Give the extent of all uninfected red blood cells.
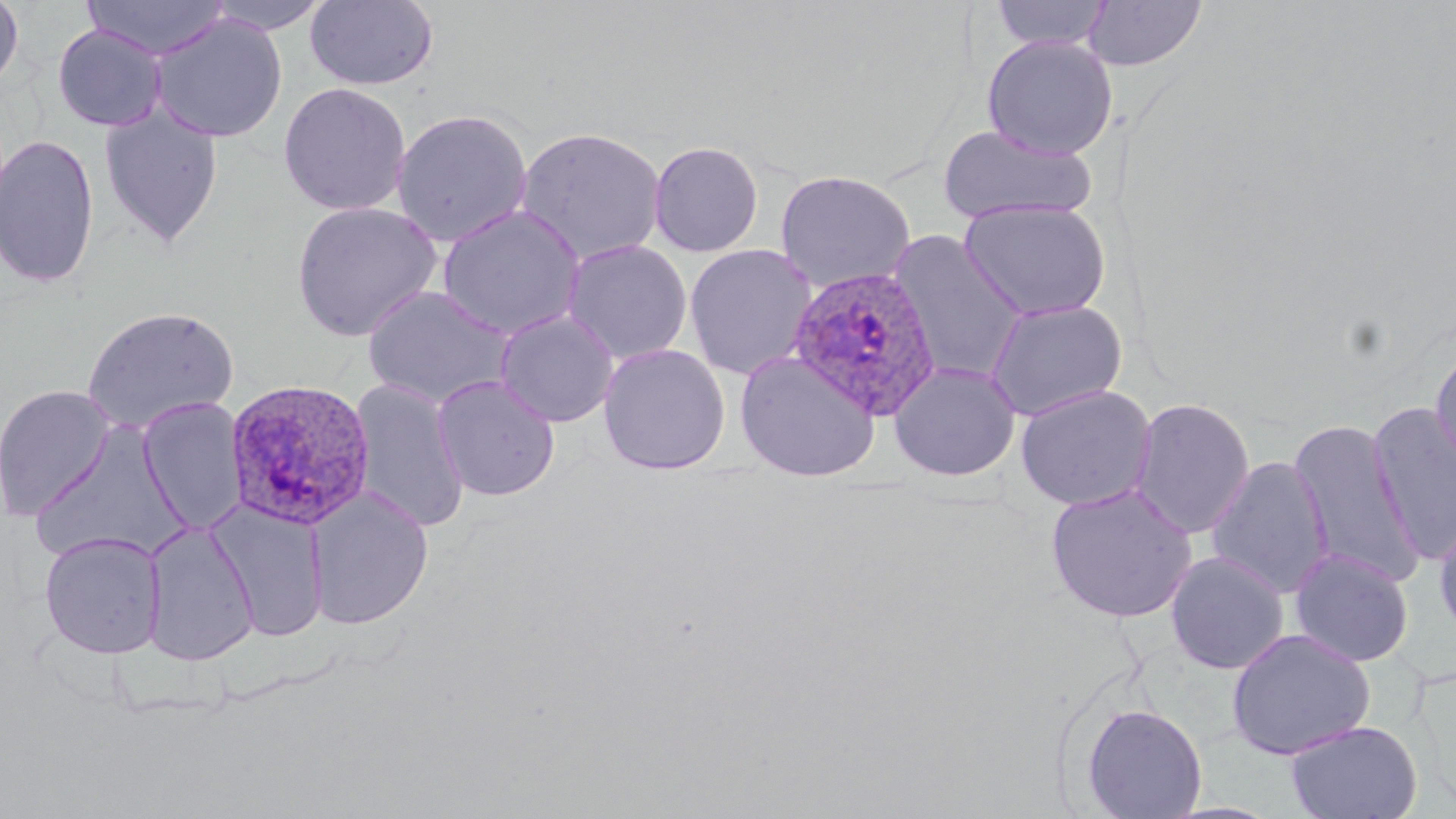

Approximate bounding boxes as named x1/y1/x2/y2 corners in pixels.
Uninfected red blood cells: (x1=0, y1=0, x2=24, y2=92), (x1=81, y1=0, x2=232, y2=59), (x1=202, y1=0, x2=333, y2=35), (x1=304, y1=0, x2=439, y2=92), (x1=990, y1=0, x2=1114, y2=50), (x1=1082, y1=1, x2=1206, y2=71), (x1=149, y1=12, x2=288, y2=143), (x1=52, y1=23, x2=167, y2=131), (x1=981, y1=35, x2=1118, y2=159), (x1=278, y1=82, x2=412, y2=216), (x1=98, y1=101, x2=224, y2=249), (x1=391, y1=108, x2=533, y2=247), (x1=937, y1=124, x2=1097, y2=226), (x1=515, y1=125, x2=667, y2=266), (x1=0, y1=134, x2=100, y2=290), (x1=648, y1=140, x2=763, y2=257), (x1=775, y1=169, x2=915, y2=292), (x1=959, y1=200, x2=1112, y2=321), (x1=291, y1=201, x2=442, y2=342), (x1=436, y1=204, x2=587, y2=340), (x1=888, y1=231, x2=1028, y2=385), (x1=562, y1=240, x2=692, y2=364), (x1=684, y1=244, x2=817, y2=380), (x1=362, y1=285, x2=516, y2=410), (x1=984, y1=298, x2=1128, y2=420), (x1=82, y1=305, x2=239, y2=434), (x1=494, y1=309, x2=619, y2=427), (x1=1429, y1=342, x2=1456, y2=473), (x1=598, y1=344, x2=730, y2=475), (x1=735, y1=350, x2=880, y2=481), (x1=889, y1=362, x2=1020, y2=481), (x1=432, y1=375, x2=561, y2=501), (x1=349, y1=379, x2=470, y2=533), (x1=0, y1=384, x2=117, y2=520), (x1=1015, y1=385, x2=1156, y2=511), (x1=1130, y1=397, x2=1255, y2=539), (x1=137, y1=398, x2=248, y2=535), (x1=1367, y1=403, x2=1456, y2=565), (x1=1288, y1=419, x2=1424, y2=587), (x1=30, y1=420, x2=191, y2=565), (x1=1206, y1=456, x2=1335, y2=599), (x1=1044, y1=483, x2=1198, y2=623), (x1=306, y1=487, x2=433, y2=629), (x1=210, y1=501, x2=330, y2=644), (x1=1433, y1=511, x2=1456, y2=644), (x1=142, y1=522, x2=258, y2=666), (x1=39, y1=531, x2=167, y2=659), (x1=1290, y1=548, x2=1414, y2=667), (x1=1165, y1=551, x2=1290, y2=675), (x1=1226, y1=628, x2=1376, y2=760), (x1=1082, y1=703, x2=1208, y2=818), (x1=1284, y1=719, x2=1422, y2=819).

Plasmodium ovale-infected red blood cell locations: (x1=786, y1=265, x2=942, y2=420), (x1=225, y1=377, x2=376, y2=531). Slide-level diagnosis: Plasmodium ovale. Thin blood smear. Single field of view. Image is 1456×819 pixels. May-Grünwald-Giemsa-stained preparation. Captured at 1000x magnification. Light microscopy.